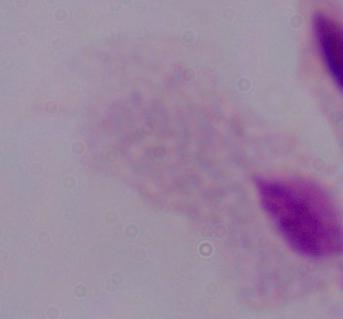

Summary:
  - Modality: photomicrograph
  - Identification: trichomonad
  - Magnification: 1000x